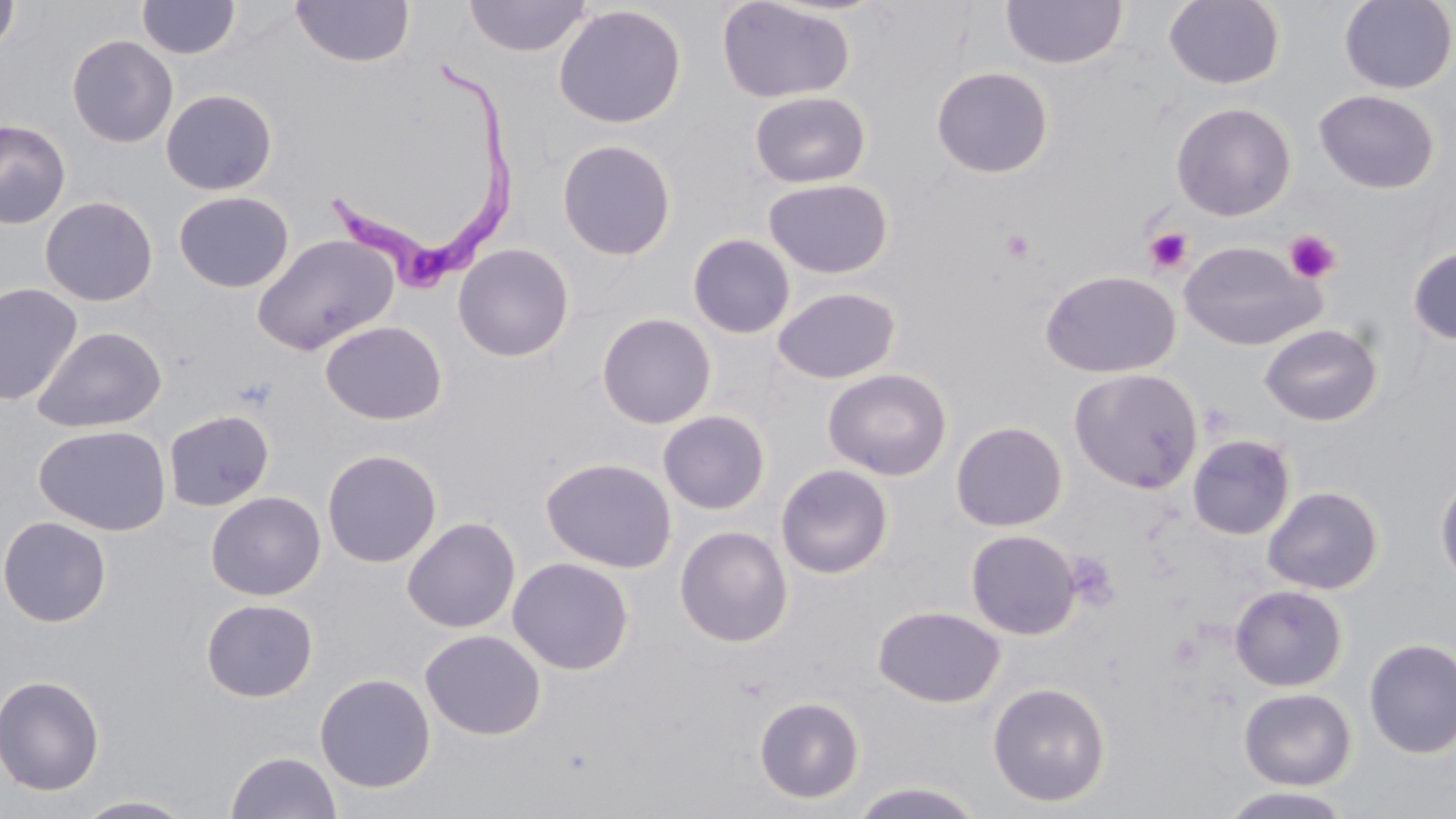
{
  "slide_level_diagnosis": "Trypanosoma brucei",
  "uninfected_red_blood_cell_locations": "approximate bounding boxes as (x1,y1)-(x2,y2) corner pairs in pixels: (463,0)-(593,58), (715,0)-(856,104), (1000,0)-(1128,70), (1164,0)-(1285,90), (1339,0)-(1455,94), (0,1)-(20,58), (137,1)-(241,60), (290,1)-(415,68), (552,4)-(688,129), (66,34)-(179,148), (930,65)-(1054,178), (160,88)-(278,196), (1314,89)-(1440,194), (748,90)-(873,189), (1171,101)-(1296,220), (0,118)-(71,229), (555,138)-(677,261), (762,177)-(894,278), (173,190)-(294,293), (40,195)-(157,307), (687,233)-(796,340), (251,234)-(399,356), (1178,240)-(1323,350), (452,243)-(575,362), (1407,246)-(1456,345), (1040,269)-(1181,378), (0,282)-(82,406), (772,286)-(901,384), (596,312)-(717,429), (320,320)-(447,426), (1259,323)-(1383,426), (32,325)-(167,433), (822,367)-(953,481), (1068,368)-(1203,493), (163,409)-(275,512), (657,410)-(771,515), (950,420)-(1068,532), (33,424)-(172,536), (1187,434)-(1296,541), (321,448)-(443,568), (541,456)-(677,573), (775,463)-(894,579), (1435,473)-(1456,587), (1262,486)-(1384,595), (205,491)-(327,600), (0,515)-(112,627), (401,516)-(521,634), (674,525)-(794,648), (965,529)-(1081,640), (506,556)-(635,675), (1229,584)-(1348,691), (200,598)-(318,702), (873,604)-(1006,708), (419,628)-(546,740), (1363,638)-(1456,759), (314,672)-(436,793), (0,675)-(105,796), (987,681)-(1111,807), (1238,687)-(1357,790), (753,696)-(865,804), (225,751)-(342,818), (848,780)-(986,818), (1213,787)-(1358,819), (71,795)-(199,818)",
  "field_of_view": "single",
  "platelet_locations": "approximate bounding boxes as (x1,y1)-(x2,y2) corner pairs in pixels: (1143,226)-(1194,276), (1000,228)-(1037,264), (1283,230)-(1342,283), (1063,551)-(1121,611)",
  "magnification": "1000x",
  "image_size": "1456×819 pixels",
  "stain": "May-Grünwald-Giemsa",
  "preparation": "thin blood film",
  "modality": "light microscopy",
  "trypanosoma_brucei_locations": "approximate bounding boxes as (x1,y1)-(x2,y2) corner pairs in pixels: (326,61)-(523,294)"
}